Give the position of each Plasmodium falciparum parasite with its life-cycle stage, each leukocyte, and any debris.
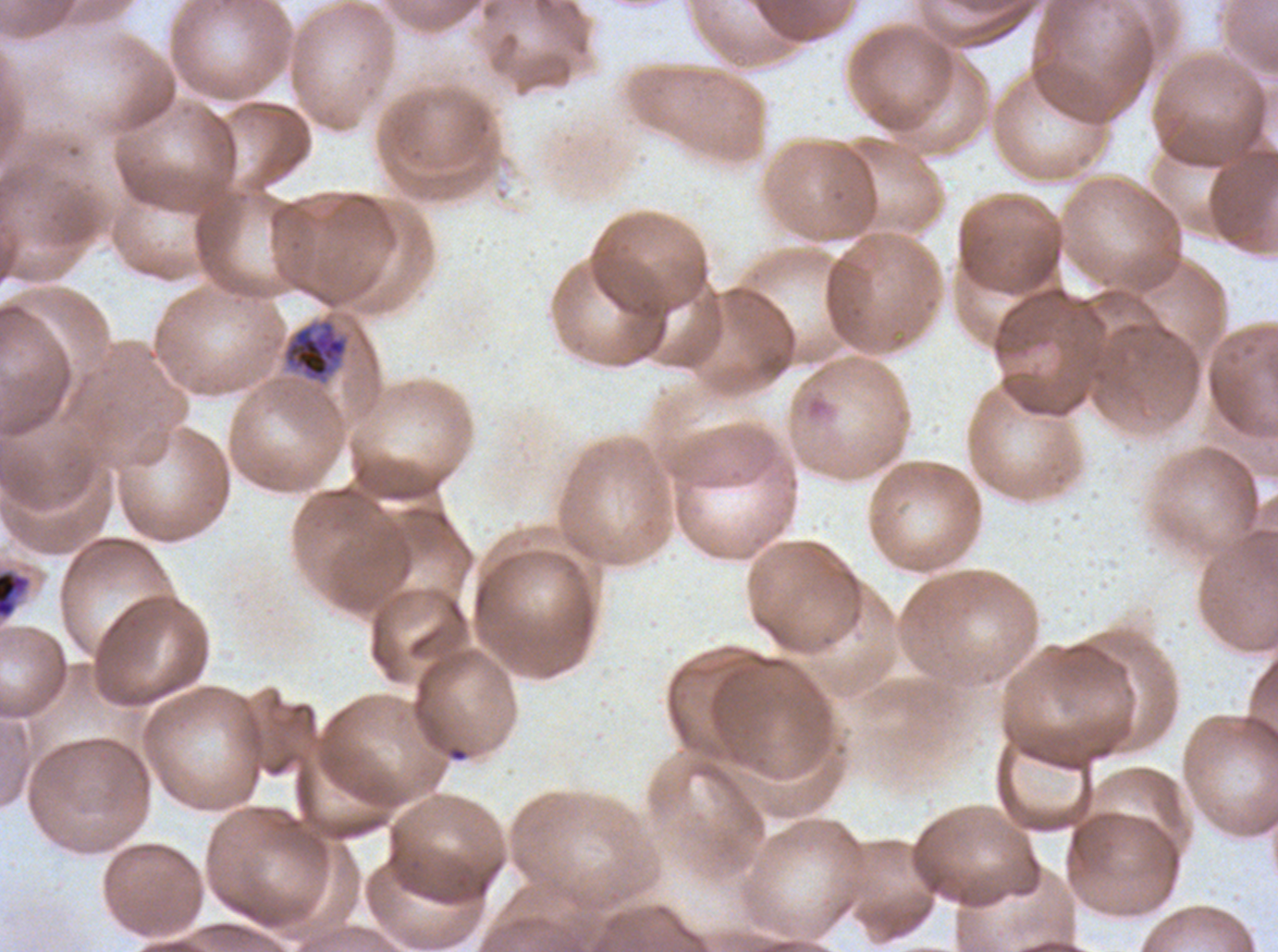
Approximate bounding rectangles given as corner coordinates in pixels from the top-left.
Late trophozoites: (x1=283, y1=319, x2=349, y2=383).
Early schizonts: (x1=0, y1=568, x2=31, y2=620).
No rings, late-ring/early-trophozoite forms, mid trophozoites, late schizonts, segmenters, gametocytes, leukocytes, or debris observed.

image size = 1278×952 pixels
life-cycle stages observed = late trophozoite, early schizont
field of view = one sub-image of a larger composite
specimen = Plasmodium falciparum cultured ex vivo for 24 to 48 hours, from a patient in The Gambia
preparation = thin blood smear
stain = Giemsa